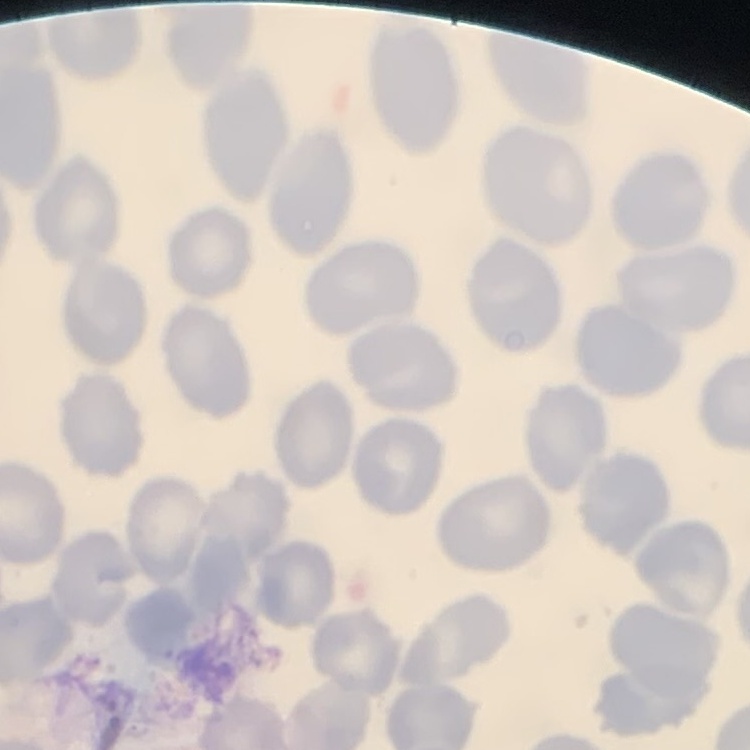
erythrocyte morphology = no rouleaux formation
stain = Field's or Giemsa
preparation = thin peripheral smear
image type = one tile cut from a larger photomicrograph